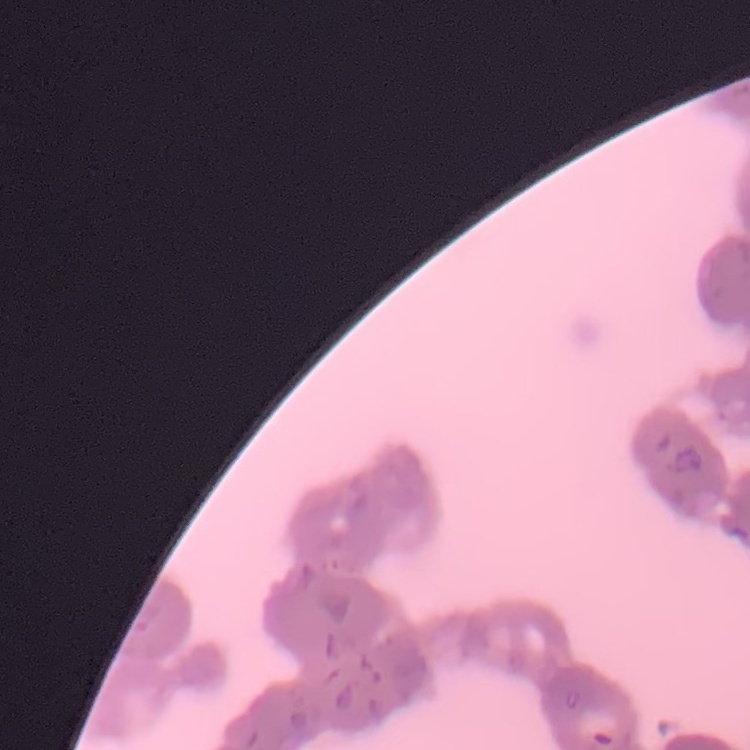

The red blood cells exhibit rouleaux formation. Thin blood film. One tile cut from a larger photomicrograph. Field's or Giemsa stain.